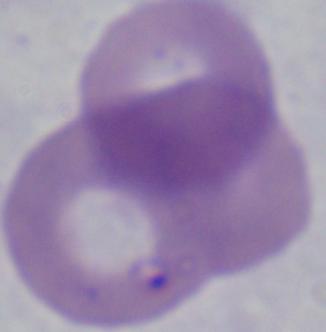

Summary:
  - Identification: Babesia
  - Modality: photomicrograph
  - Magnification: 1000x